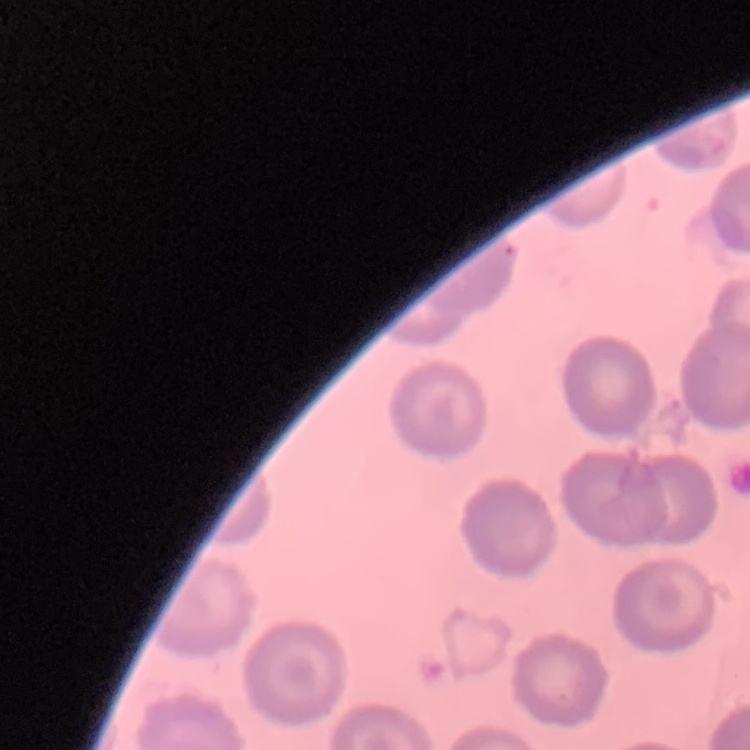

Summary:
  - Red blood cell morphology: no rouleaux formation
  - Preparation: thin peripheral smear
  - Image type: square crop of a larger photomicrograph
  - Stain: Field's or Giemsa